Mark where platelets are.
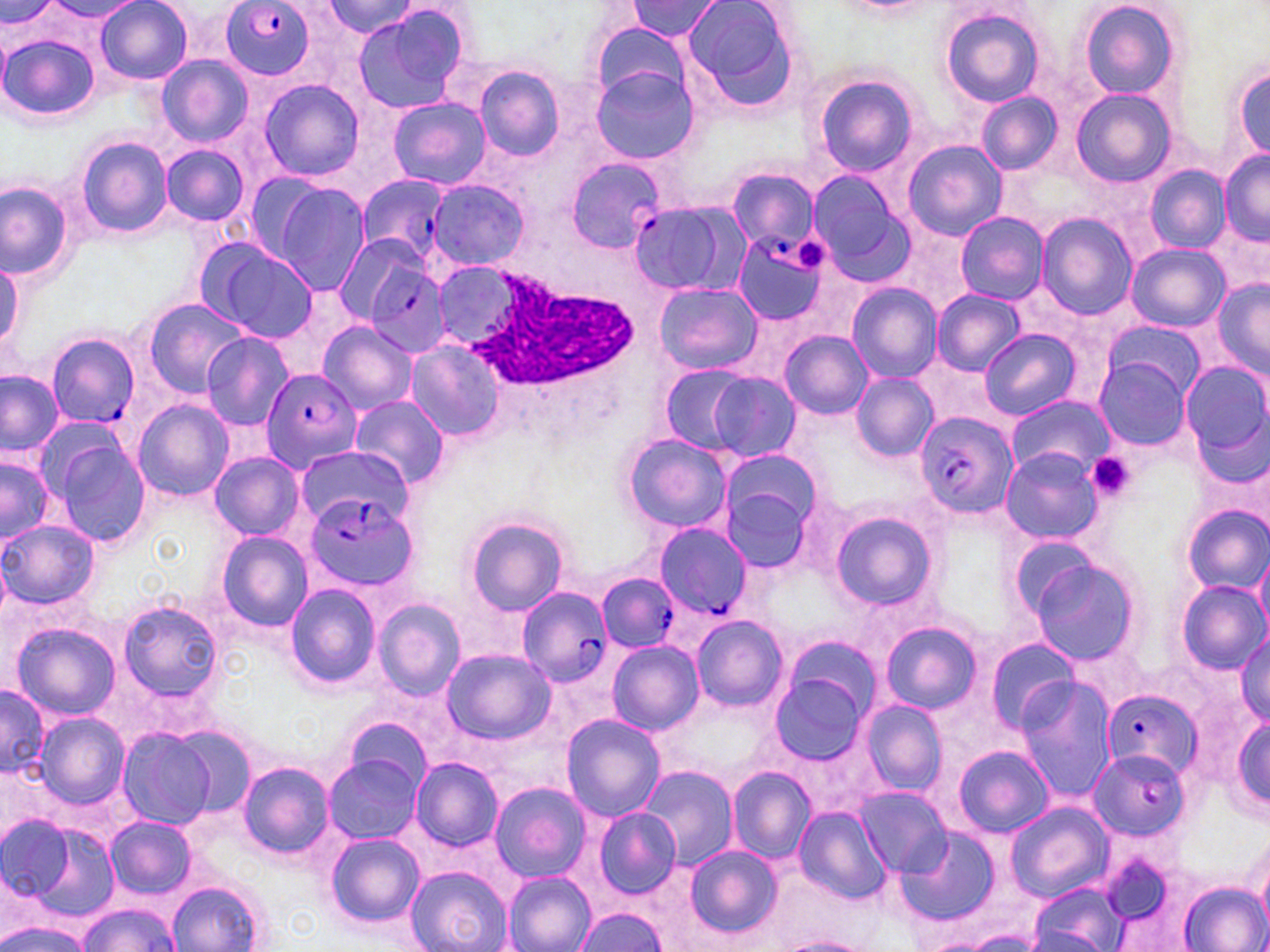
Approximate bounding boxes as (x1, y1, x2, y2) in pixels.
Platelets: (797, 238, 827, 273), (1089, 455, 1138, 498).

Summary:
  - Plasmodium falciparum-infected red blood cell locations: (218, 1, 319, 80), (564, 156, 664, 253), (357, 175, 449, 266), (635, 199, 741, 300), (735, 233, 833, 325), (360, 257, 455, 358), (47, 335, 141, 426), (261, 370, 363, 474), (914, 410, 1018, 520), (303, 493, 418, 592), (656, 523, 754, 621), (598, 573, 679, 652), (517, 586, 612, 687), (1101, 689, 1201, 780), (1088, 750, 1191, 842)
  - Uninfected red blood cell locations: (630, 0, 721, 41), (4, 1, 58, 33), (680, 1, 799, 105), (1081, 1, 1180, 99), (47, 2, 144, 23), (96, 2, 192, 83), (324, 2, 422, 40), (941, 7, 1045, 108), (352, 8, 469, 114), (589, 22, 690, 102), (2, 33, 100, 122), (156, 55, 253, 148), (1229, 57, 1270, 165), (471, 63, 568, 163), (592, 67, 698, 165), (815, 75, 917, 177), (258, 78, 365, 182), (1071, 89, 1174, 186), (977, 94, 1062, 173), (389, 97, 489, 188), (74, 135, 173, 239), (903, 140, 1007, 241), (160, 144, 250, 226), (1220, 151, 1269, 245), (1144, 164, 1230, 254), (728, 167, 817, 254), (806, 169, 912, 281), (242, 171, 331, 263), (427, 179, 529, 271), (0, 182, 75, 279), (271, 183, 372, 296), (954, 212, 1048, 305), (1036, 213, 1137, 318), (331, 231, 432, 329), (199, 243, 319, 345), (1124, 243, 1230, 331), (0, 264, 25, 360), (1212, 279, 1269, 377), (655, 283, 763, 374), (847, 283, 942, 383), (930, 289, 1023, 377), (142, 298, 249, 396), (317, 320, 416, 414), (1101, 321, 1205, 399), (978, 327, 1080, 420), (780, 330, 874, 419), (200, 331, 293, 432), (404, 340, 505, 441), (1093, 359, 1193, 449), (1179, 361, 1270, 466), (657, 364, 764, 454), (0, 370, 64, 457), (704, 371, 801, 462), (851, 372, 937, 462), (1006, 394, 1113, 477), (349, 397, 449, 489), (133, 399, 235, 502), (40, 430, 153, 551), (620, 433, 731, 534), (298, 442, 416, 516), (718, 448, 822, 538), (1000, 448, 1108, 545), (210, 452, 304, 541), (0, 453, 55, 549), (719, 481, 817, 572), (1179, 504, 1270, 595), (828, 509, 937, 611), (465, 517, 568, 616), (1, 520, 98, 611), (217, 531, 313, 632), (1255, 547, 1270, 636), (1026, 557, 1142, 665), (1175, 580, 1269, 675), (285, 584, 381, 690), (373, 599, 466, 699), (117, 600, 224, 703), (691, 615, 787, 710), (878, 620, 982, 716), (13, 622, 122, 721), (1235, 629, 1270, 727), (779, 635, 881, 725), (983, 636, 1082, 734), (607, 640, 703, 737), (440, 649, 554, 745), (768, 672, 871, 768), (1013, 679, 1116, 802), (0, 682, 48, 782), (859, 697, 949, 799), (35, 713, 129, 811), (561, 714, 663, 821), (1225, 715, 1270, 820), (345, 717, 432, 792), (172, 726, 258, 819), (117, 728, 218, 831), (953, 746, 1054, 837), (323, 753, 422, 845), (410, 753, 511, 944), (412, 757, 503, 850), (236, 760, 335, 861), (641, 766, 736, 869), (728, 766, 814, 863), (488, 781, 591, 883), (855, 788, 950, 878), (1006, 801, 1112, 899), (792, 806, 893, 904), (593, 809, 680, 896), (0, 816, 75, 904), (104, 818, 196, 899), (16, 819, 121, 924), (894, 827, 1001, 926), (324, 832, 424, 928), (679, 843, 785, 943), (1254, 846, 1270, 939), (406, 866, 511, 952), (502, 872, 595, 952), (166, 878, 270, 952), (1027, 880, 1129, 952), (1177, 880, 1270, 952), (75, 904, 177, 952), (570, 907, 670, 951), (2, 917, 91, 952), (775, 936, 873, 952)
  - White blood cell locations: (466, 269, 641, 391)
  - Slide-level diagnosis: Plasmodium falciparum
  - Field of view: one of a larger specimen
  - Stain: May-Grünwald-Giemsa
  - Preparation: thin blood film
  - Magnification: 1000x
  - Image size: 1270×952 pixels
  - Modality: optical microscopy